Report the malaria status of this cell.
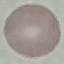

Uninfected.

Summary:
  - Capture: smartphone camera at the microscope eyepiece
  - Image type: cell patch, automatically extracted from a larger field of view and resized to 64 × 64 pixels
  - Preparation: thin smear
  - Stain: Giemsa